Point out each Plasmodium parasite.
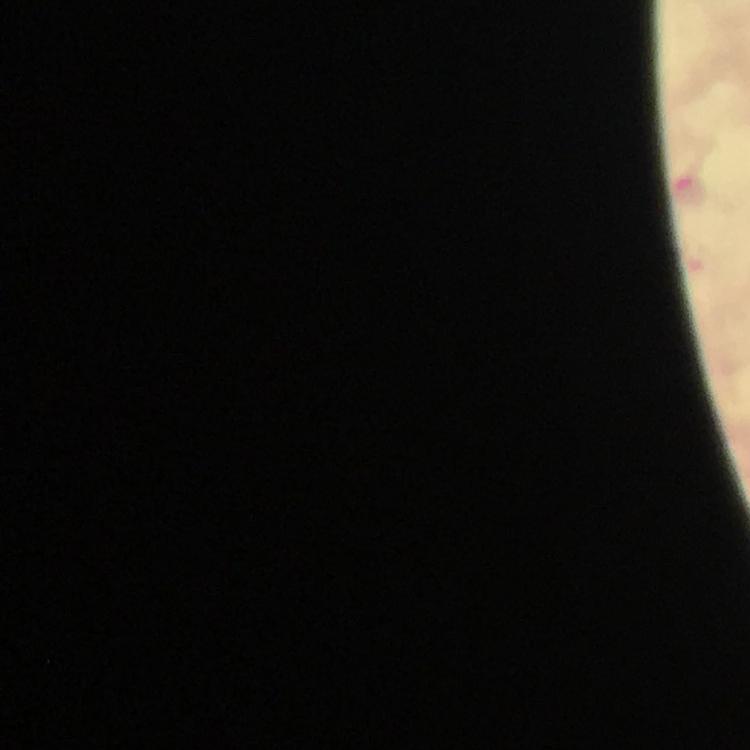
Approximate centers as [x, y] in pixels.
Plasmodium parasites: [688, 188].

Summary:
  - Capture: smartphone camera through the microscope
  - Image size: 750×750 pixels
  - Magnification: 100x
  - Preparation: thick smear
  - Cropped from: a single field of view
  - Context: from a diagnostic examination for malaria
  - Immersion oil: applied
  - Stain: Giemsa